Give the position of every Plasmodium parasite.
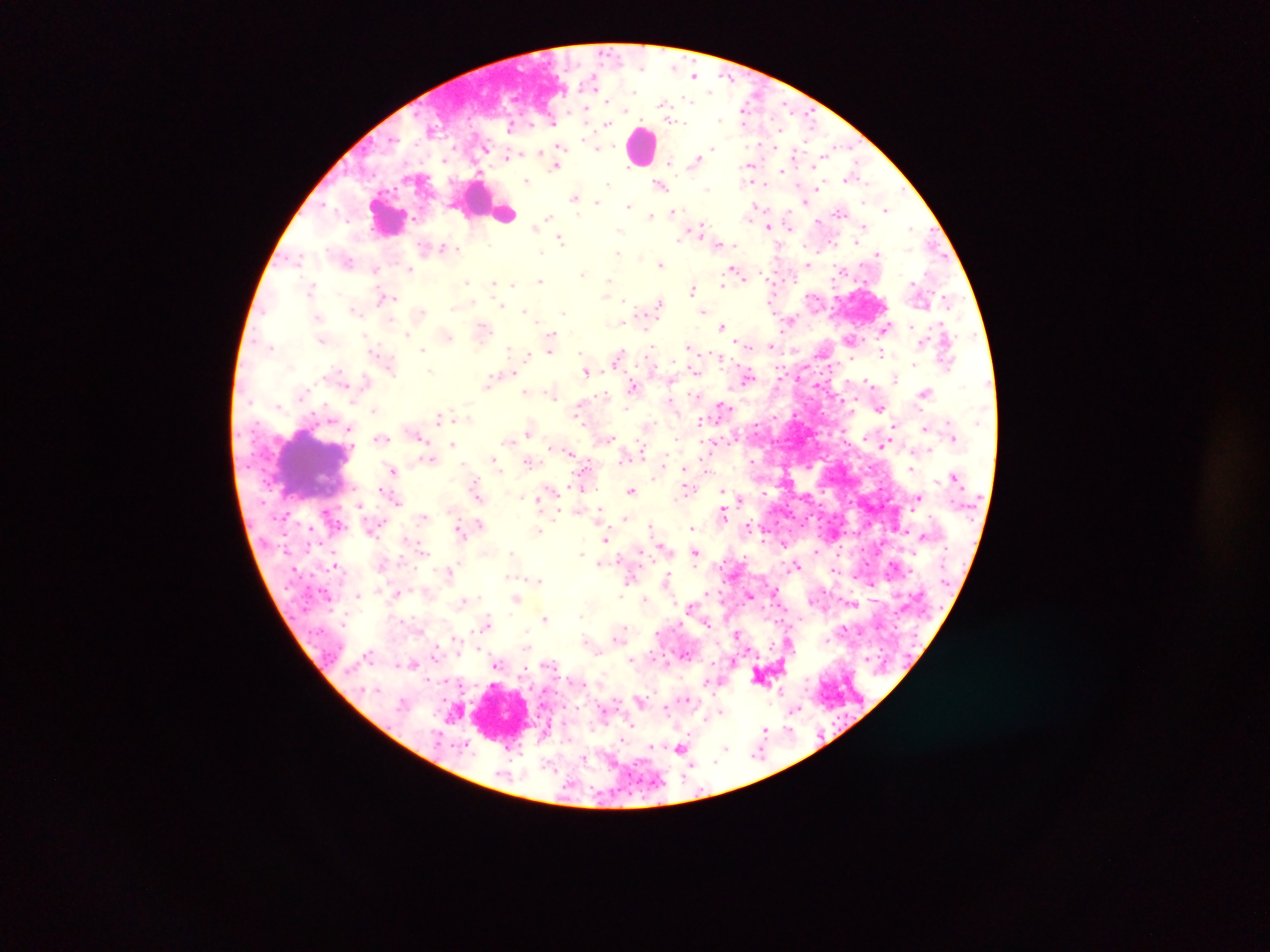

Approximate centers as (x, y) in pixels.
Plasmodium parasites: (695, 75), (593, 81), (688, 100), (663, 104), (745, 106), (786, 106), (585, 112), (809, 118), (720, 119), (674, 121), (553, 122), (678, 122), (608, 124), (431, 129), (598, 147), (486, 148), (560, 148), (712, 148), (511, 155), (696, 160), (670, 162), (556, 165), (750, 165), (782, 170), (479, 173), (850, 177), (527, 181), (609, 184), (660, 185), (817, 188), (707, 189), (574, 197), (596, 202), (803, 202), (326, 205), (629, 206), (756, 207), (887, 210), (674, 211), (841, 212), (650, 215), (548, 218), (818, 222), (534, 226), (768, 226), (789, 226), (864, 226), (911, 228), (699, 230), (680, 238), (561, 239), (856, 241), (719, 245), (445, 248), (456, 248), (617, 253), (878, 253), (298, 257), (349, 261), (660, 264), (808, 265), (410, 269), (734, 269), (375, 270), (583, 274), (540, 280), (608, 281), (467, 282), (726, 282), (493, 283), (513, 284), (723, 285), (311, 288), (693, 289), (385, 298), (624, 300), (772, 300), (659, 303), (501, 305), (454, 307), (355, 310), (525, 311), (704, 311), (421, 312), (563, 312), (789, 322), (620, 323), (723, 326), (484, 327), (886, 327), (910, 327), (406, 333), (552, 336), (448, 337), (850, 339), (744, 344), (651, 346), (688, 346), (770, 346), (271, 347), (422, 349), (510, 350), (550, 351), (527, 354), (882, 354), (618, 356), (914, 364), (389, 367), (694, 370), (429, 371), (586, 372), (512, 373), (748, 376), (895, 379), (366, 380), (868, 381), (489, 382), (633, 386), (525, 392), (925, 392), (551, 394), (604, 395), (579, 406), (723, 406), (880, 408), (373, 410), (439, 416), (700, 423), (894, 425), (925, 428), (348, 429), (529, 431), (419, 437), (610, 437), (381, 438), (509, 440), (452, 444), (884, 445), (641, 447), (570, 453), (431, 459), (495, 459), (752, 461), (530, 462), (685, 469), (910, 469), (393, 470), (476, 487), (581, 487), (553, 489), (632, 490), (686, 491), (723, 491), (477, 494), (522, 497), (739, 498), (919, 498), (397, 501), (360, 505), (600, 511), (723, 512), (556, 514), (424, 517), (625, 517), (479, 523), (650, 525), (749, 525), (692, 527), (458, 528), (538, 531), (922, 535), (606, 539), (784, 544), (662, 546), (423, 550), (816, 551), (640, 552), (511, 553), (695, 553), (582, 554), (601, 563), (334, 565), (797, 565), (451, 571), (509, 576), (631, 577), (668, 577), (539, 580), (872, 584), (398, 593), (358, 595), (621, 596), (749, 596), (515, 599), (644, 600), (464, 601), (690, 606), (581, 616), (545, 617), (488, 623), (707, 624), (624, 629), (737, 634), (586, 640), (527, 648), (369, 654), (414, 664), (497, 664), (640, 699), (666, 707), (796, 709), (721, 712), (630, 725), (764, 729), (788, 729), (651, 747), (725, 748), (680, 749), (757, 754), (584, 758), (658, 781).

Summary:
  - Leukocyte locations: (643, 145), (505, 213), (386, 217), (313, 470), (505, 712)
  - Preparation: thick blood film
  - Image size: 1270×952 pixels
  - Field of view: single
  - Country: Ghana
  - Capture: mobile-phone photograph through a microscope